Identify the cell.
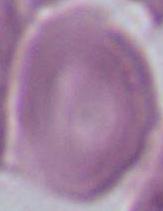
An erythrocyte.

Photomicrograph. Captured at 1000x magnification.